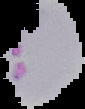

Malaria status: uninfected. Image is 85×109 pixels. From a thin blood smear. Cell region segmented out of the field of view; the surrounding area is masked to black.